Outline each blood parasite and name the species.
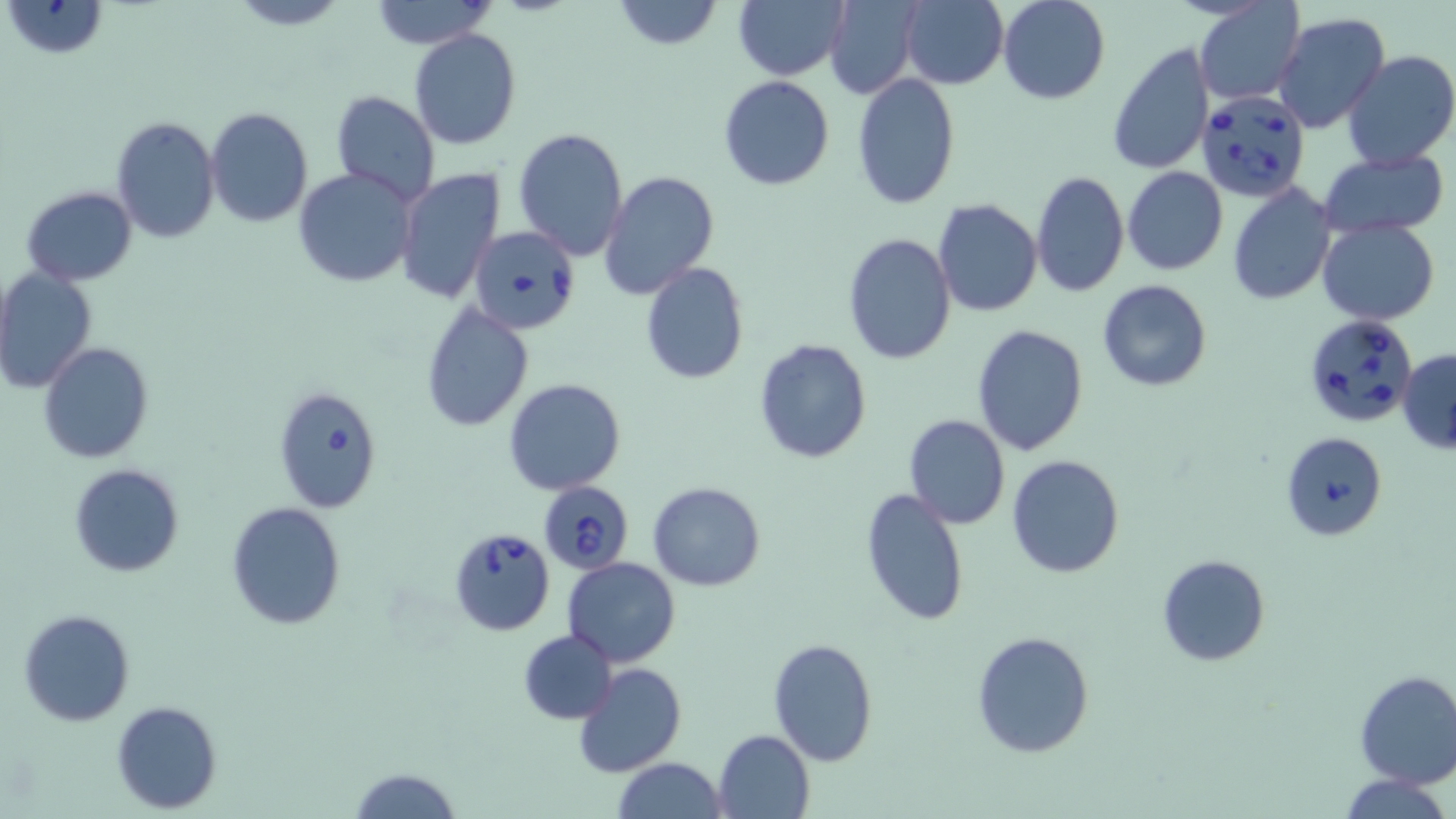
Approximate bounding boxes as [x1, y1, x2, y2] in pixels.
Babesia divergens-infected red blood cells: [1197, 89, 1313, 203], [468, 225, 581, 336], [1303, 313, 1419, 428], [273, 384, 385, 512], [1280, 432, 1388, 540], [537, 480, 634, 575], [448, 526, 555, 637].
No Plasmodium falciparum, Plasmodium ovale, Plasmodium malariae, Plasmodium vivax, or Trypanosoma brucei observed.

Uninfected red blood cell locations: [3, 0, 110, 59], [225, 0, 351, 30], [368, 0, 495, 49], [612, 0, 724, 51], [733, 0, 848, 81], [823, 0, 922, 101], [901, 0, 1009, 89], [997, 0, 1109, 104], [1194, 2, 1306, 106], [1272, 12, 1392, 135], [409, 29, 521, 150], [1106, 42, 1215, 175], [1341, 50, 1456, 170], [850, 73, 960, 211], [718, 75, 835, 190], [331, 90, 441, 208], [206, 106, 312, 228], [111, 116, 222, 244], [514, 128, 630, 262], [1320, 149, 1449, 235], [1122, 165, 1229, 276], [292, 166, 418, 288], [395, 167, 506, 303], [599, 169, 721, 302], [1030, 171, 1130, 297], [1227, 184, 1337, 303], [21, 185, 137, 286], [934, 199, 1042, 317], [1317, 220, 1440, 325], [842, 232, 957, 365], [641, 261, 750, 384], [0, 267, 97, 394], [1096, 279, 1212, 392], [421, 300, 534, 431], [971, 324, 1089, 456], [754, 338, 872, 463], [38, 342, 154, 464], [1398, 348, 1456, 453], [504, 378, 628, 496], [903, 414, 1010, 529], [1006, 454, 1126, 578], [69, 463, 185, 577], [648, 481, 766, 592], [860, 488, 970, 629], [226, 502, 346, 629], [1156, 554, 1271, 666], [563, 557, 679, 667], [17, 608, 136, 727], [519, 630, 617, 724], [971, 631, 1095, 758], [767, 637, 879, 766], [572, 662, 685, 778], [1353, 671, 1456, 788], [111, 699, 223, 814], [714, 729, 815, 818], [613, 758, 727, 818], [350, 767, 461, 818], [1340, 773, 1452, 819]. Slide-level diagnosis: Babesia divergens. Single field of view. May-Grünwald-Giemsa-stained preparation. Image is 1456×819 pixels. Light microscopy. Thin blood film. Captured at 1000x magnification.